Give the location of every white blood cell.
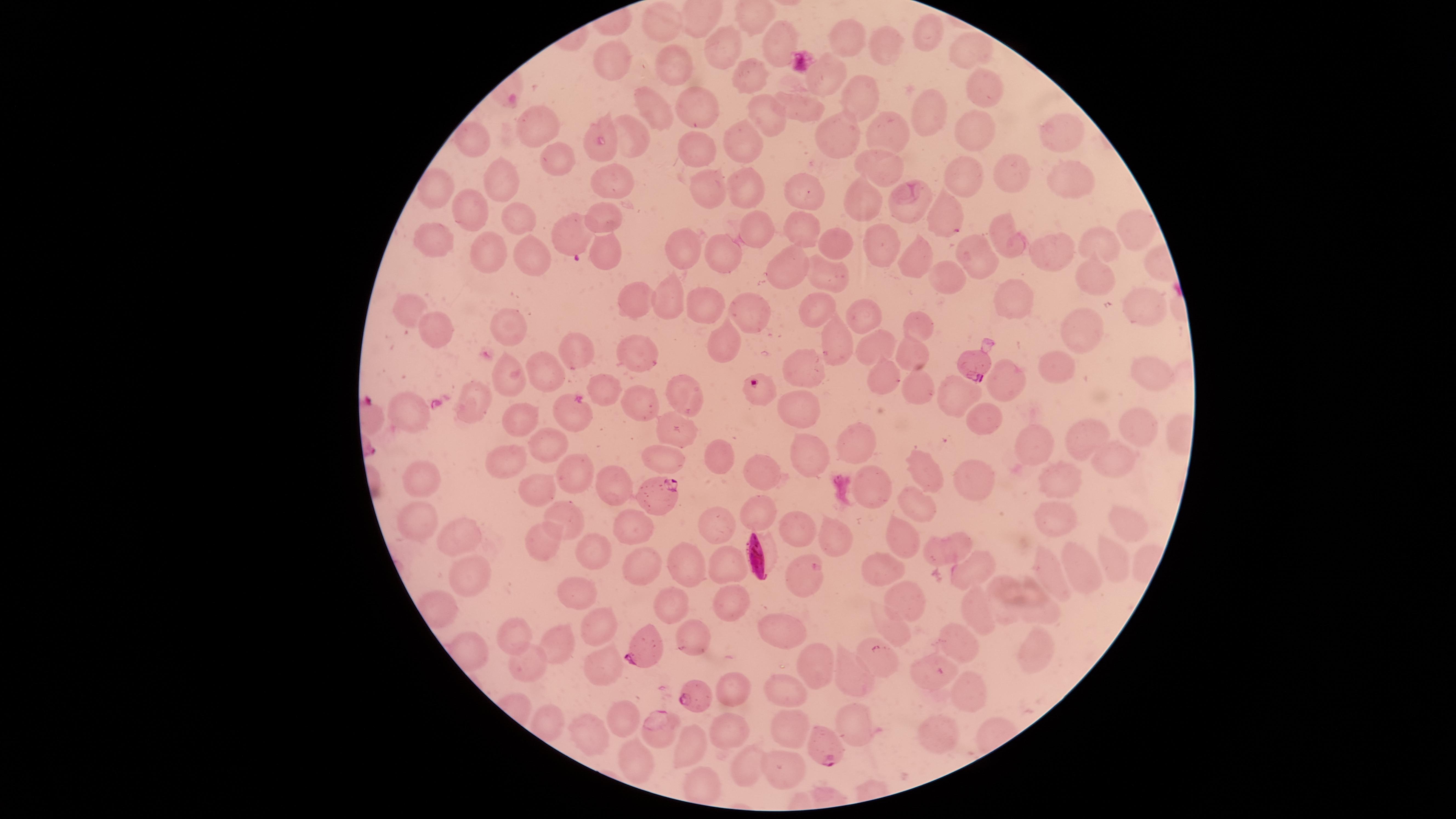
No white blood cells identified.

Approximate marker points as {x, y} in pixels. Uninfected red blood cells: {664, 23}, {920, 30}, {848, 35}, {775, 45}, {726, 47}, {882, 47}, {969, 50}, {613, 55}, {675, 64}, {821, 79}, {748, 81}, {981, 83}, {860, 96}, {798, 103}, {927, 106}, {703, 107}, {647, 108}, {761, 118}, {602, 127}, {1059, 127}, {875, 128}, {535, 130}, {971, 130}, {839, 132}, {637, 137}, {472, 141}, {694, 144}, {745, 144}, {560, 157}, {879, 161}, {1009, 173}, {608, 176}, {960, 176}, {1067, 178}, {501, 181}, {746, 185}, {710, 186}, {438, 187}, {804, 195}, {863, 200}, {907, 206}, {471, 208}, {609, 212}, {946, 213}, {509, 214}, {1131, 225}, {800, 226}, {755, 230}, {1001, 230}, {441, 234}, {1094, 241}, {684, 244}, {883, 244}, {836, 247}, {1048, 249}, {727, 251}, {479, 253}, {533, 254}, {603, 254}, {976, 255}, {794, 259}, {914, 259}, {829, 273}, {1099, 277}, {944, 278}, {1016, 295}, {644, 297}, {668, 297}, {1142, 298}, {707, 302}, {808, 302}, {412, 309}, {747, 313}, {863, 314}, {913, 322}, {513, 325}, {441, 329}, {1084, 329}, {832, 337}, {722, 341}, {875, 345}, {912, 349}, {574, 350}, {637, 351}, {550, 364}, {1062, 365}, {809, 366}, {1143, 367}, {512, 375}, {885, 378}, {1012, 380}, {609, 383}, {923, 385}, {681, 386}, {965, 389}, {639, 401}, {474, 402}, {570, 413}, {803, 413}, {408, 415}, {524, 416}, {987, 420}, {1134, 422}, {673, 431}, {1088, 436}, {857, 438}, {546, 440}, {1038, 443}, {809, 456}, {1112, 456}, {505, 457}, {662, 459}, {717, 459}, {924, 466}, {578, 472}, {764, 474}, {422, 477}, {1053, 481}, {613, 482}, {969, 482}, {872, 486}, {538, 491}, {913, 503}, {1051, 514}, {764, 515}, {420, 519}, {568, 520}, {1126, 522}, {629, 525}, {793, 529}, {833, 533}, {905, 535}, {711, 536}, {461, 538}, {541, 542}, {596, 550}, {953, 551}, {1112, 554}, {694, 555}, {641, 562}, {727, 562}, {978, 566}, {881, 569}, {1073, 569}, {1052, 570}, {468, 576}, {805, 579}, {578, 593}, {910, 596}, {671, 603}, {728, 603}, {1004, 605}, {1040, 607}, {892, 628}, {517, 629}, {597, 629}, {789, 632}, {700, 638}, {561, 640}, {954, 640}, {1030, 650}, {533, 656}, {877, 662}, {601, 664}, {809, 664}, {932, 673}, {849, 676}, {974, 688}, {733, 689}, {788, 690}, {620, 717}, {857, 720}, {788, 726}, {588, 727}, {940, 729}, {732, 731}, {658, 733}, {689, 744}, {635, 759}, {782, 768}, {744, 771}. Parasitized red blood cells: {570, 236}, {975, 368}, {759, 388}, {664, 492}, {648, 641}, {696, 694}, {820, 744}. Giemsa stain. Species: Plasmodium falciparum. The visible region is circular. Image is 1456×819 pixels. Photographed with a smartphone camera through the microscope eyepiece. Thin blood film. Presence: malaria parasites identified. Single field of view.